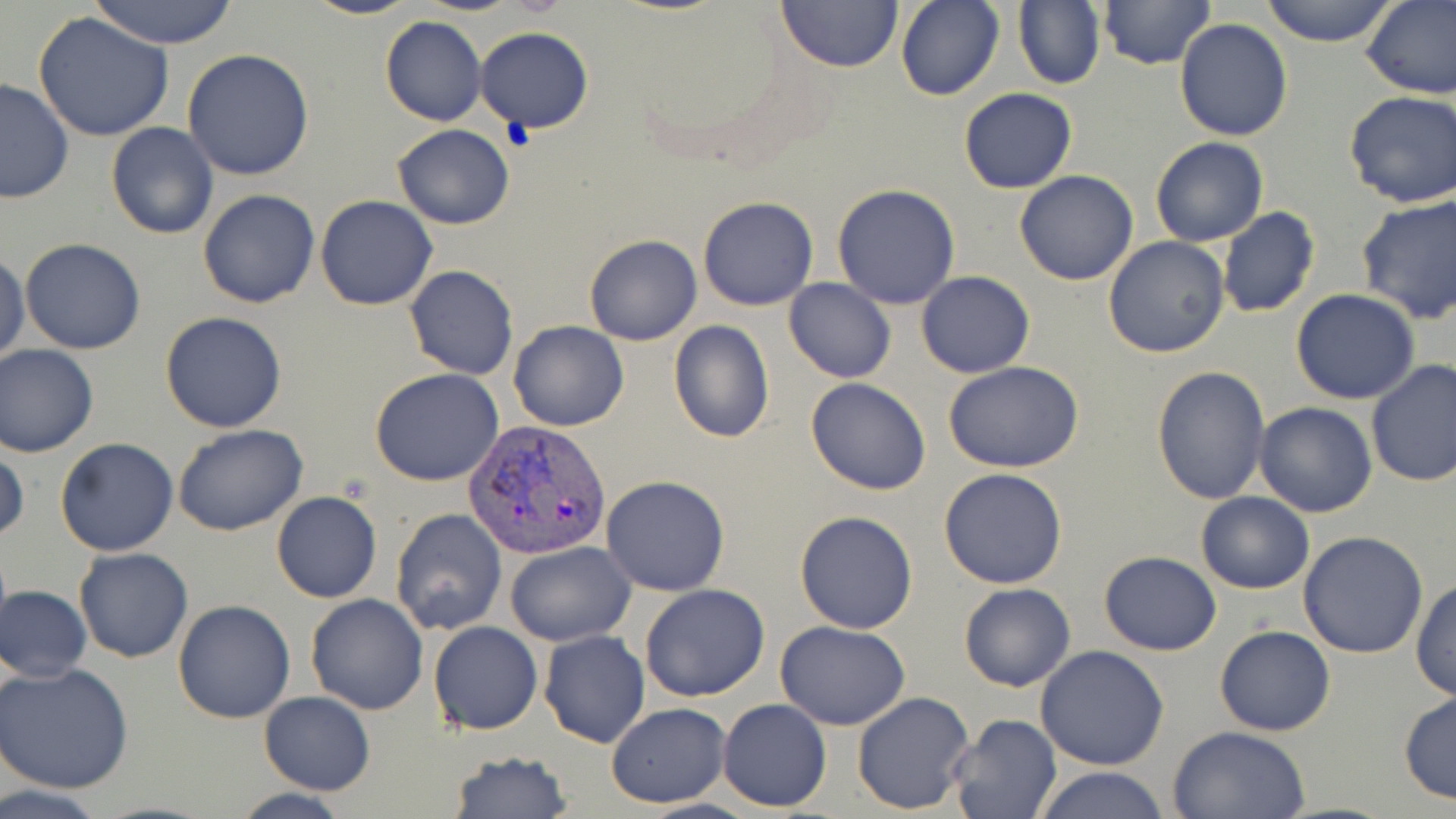
slide_level_diagnosis: Plasmodium vivax
image_size: 1456×819 pixels
stain: May-Grünwald-Giemsa
plasmodium_vivax_infected_red_blood_cell_locations: 'approximate bounding boxes as [x1, y1, x2, y2] in pixels: [464, 419, 613, 561]'
modality: optical microscopy
magnification: 1000x
field_of_view: single
uninfected_red_blood_cell_locations: 'approximate bounding boxes as [x1, y1, x2, y2] in pixels: [88, 0, 241, 47], [301, 0, 423, 20], [777, 0, 902, 71], [896, 0, 1004, 101], [1013, 0, 1105, 91], [1259, 0, 1401, 47], [1360, 0, 1456, 100], [1097, 1, 1215, 70], [32, 9, 176, 142], [380, 16, 486, 127], [1174, 18, 1292, 140], [476, 25, 594, 132], [183, 48, 314, 180], [0, 77, 76, 205], [957, 87, 1077, 194], [1343, 92, 1456, 208], [106, 122, 219, 240], [392, 124, 514, 230], [1151, 137, 1268, 247], [1014, 170, 1139, 286], [832, 183, 961, 309], [198, 190, 321, 309], [1355, 193, 1456, 324], [315, 195, 437, 310], [697, 196, 819, 312], [1217, 206, 1320, 318], [583, 234, 702, 346], [1102, 235, 1230, 359], [20, 238, 146, 354], [0, 252, 28, 366], [404, 265, 519, 381], [927, 270, 1057, 468], [917, 272, 1035, 377], [784, 278, 896, 383], [1290, 290, 1421, 404], [159, 310, 288, 433], [508, 321, 630, 431], [667, 321, 776, 443], [0, 345, 99, 458], [1366, 359, 1456, 487], [944, 360, 1084, 472], [1151, 364, 1270, 503], [369, 367, 504, 486], [805, 377, 931, 495], [1254, 402, 1378, 517], [173, 423, 307, 535], [55, 437, 179, 556], [1, 444, 28, 547], [940, 466, 1069, 588], [601, 475, 730, 595], [271, 492, 382, 604], [1195, 492, 1315, 594], [390, 507, 507, 634], [795, 510, 918, 635], [1298, 531, 1429, 659], [505, 541, 635, 646], [74, 548, 194, 663], [1098, 551, 1222, 656], [1411, 576, 1456, 701], [958, 582, 1076, 692], [640, 583, 770, 702], [2, 584, 92, 683], [305, 593, 430, 714], [172, 601, 295, 723], [428, 621, 543, 735], [776, 621, 912, 730], [1215, 624, 1335, 737], [540, 630, 650, 748], [1035, 645, 1169, 770], [0, 663, 134, 793], [1399, 689, 1456, 804], [851, 690, 975, 815], [259, 692, 374, 794], [717, 699, 832, 812], [606, 703, 730, 808], [945, 713, 1063, 819], [1168, 727, 1309, 818], [449, 751, 572, 818], [1030, 766, 1170, 819], [0, 784, 112, 819], [230, 789, 358, 819]'
preparation: thin blood film